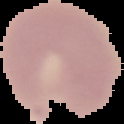 The area outside the segmented cell region is set to black. Image is 124×124 pixels. Malaria status: parasitized. From a thin blood smear.